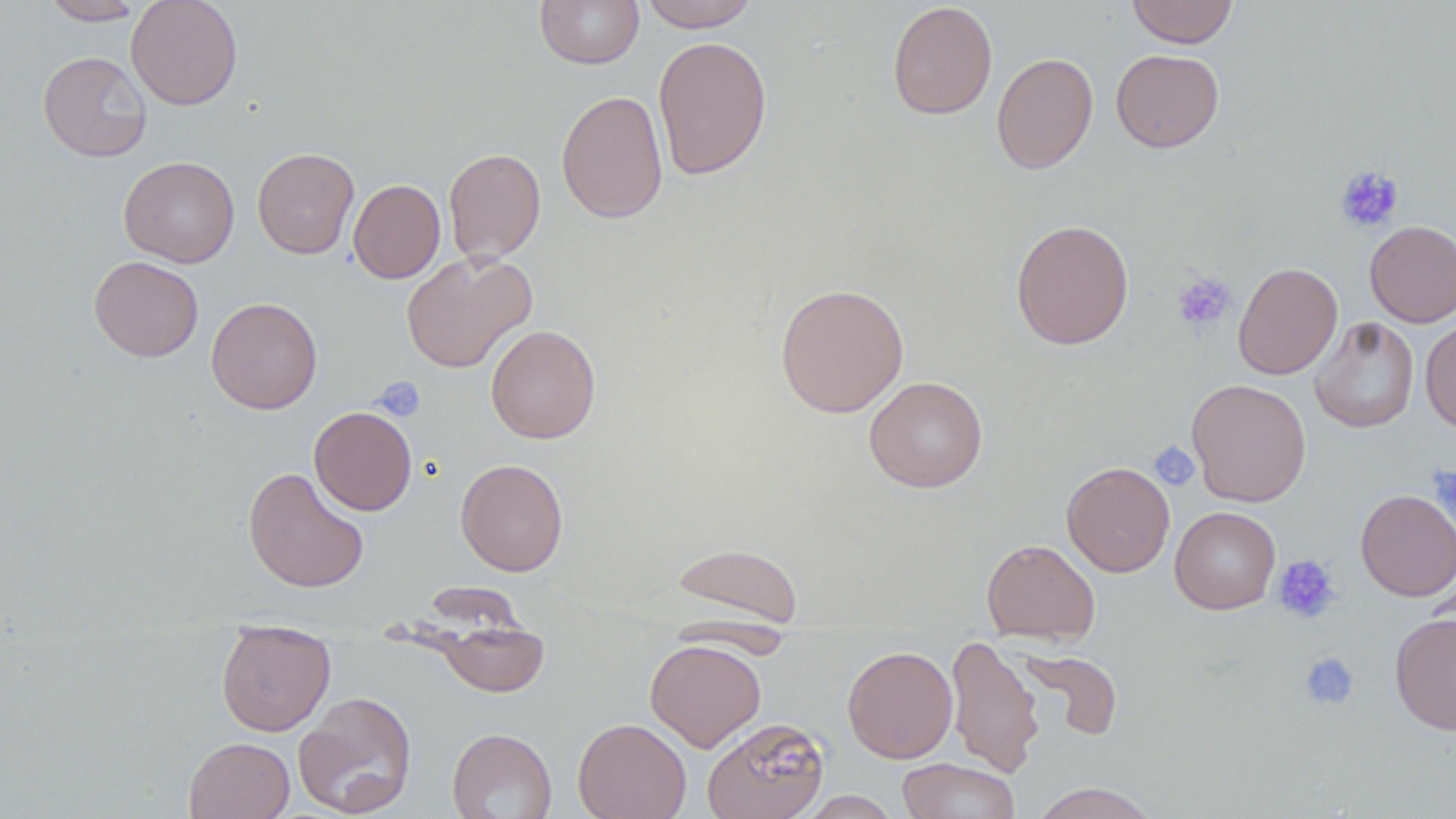
slide-level diagnosis = no evidence of blood parasites
platelet locations = approximate bounding boxes as (x1, y1, x2, y2) in pixels: (1334, 165, 1404, 233), (1172, 272, 1236, 331), (373, 377, 425, 422), (1148, 441, 1199, 491), (1431, 464, 1456, 527), (1273, 554, 1342, 624), (1298, 651, 1359, 711)
magnification = 1000x
image size = 1456×819 pixels
modality = light microscopy
uninfected red blood cell locations = approximate bounding boxes as (x1, y1, x2, y2) in pixels: (41, 0, 145, 25), (126, 0, 243, 110), (535, 0, 644, 69), (636, 0, 760, 31), (1126, 0, 1238, 48), (887, 2, 998, 119), (653, 35, 772, 181), (1111, 49, 1224, 152), (38, 51, 152, 162), (991, 51, 1098, 174), (556, 90, 668, 224), (252, 147, 359, 259), (443, 148, 546, 264), (119, 156, 239, 268), (348, 179, 445, 283), (1011, 219, 1133, 349), (1364, 220, 1456, 327), (401, 251, 537, 373), (88, 255, 204, 362), (1233, 262, 1342, 380), (774, 282, 909, 418), (206, 297, 322, 414), (1309, 316, 1419, 433), (1420, 316, 1456, 433), (486, 324, 600, 443), (864, 376, 988, 492), (1187, 379, 1311, 506), (309, 406, 417, 515), (456, 458, 569, 576), (1061, 461, 1175, 577), (243, 467, 369, 593), (1356, 489, 1456, 601), (1169, 506, 1281, 614), (982, 538, 1100, 645), (671, 542, 803, 628), (1389, 612, 1456, 735), (435, 619, 550, 698), (216, 627, 335, 737), (944, 634, 1044, 776), (645, 639, 766, 752), (842, 645, 957, 763), (1018, 648, 1123, 741), (293, 691, 417, 818), (573, 717, 691, 819), (702, 717, 829, 819), (447, 728, 557, 819), (184, 737, 295, 819), (898, 758, 1021, 819), (1029, 782, 1160, 819), (797, 791, 901, 818)
field of view = one of a larger specimen
preparation = thin blood film
stain = May-Grünwald-Giemsa